Report the malaria status of this cell.
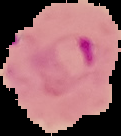

Parasitized.

image size = 121×136 pixels
image type = segmented cell region on a black background
preparation = thin blood film